Assess the morphology of the erythrocytes.
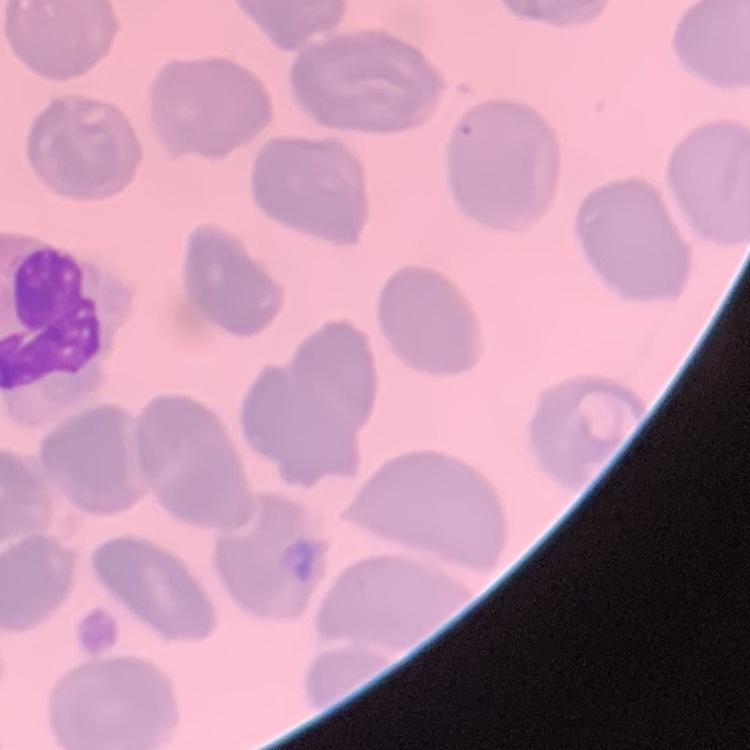
They show no rouleaux formation.

Field's or Giemsa stain. Square crop of a larger photomicrograph. Thin blood film.